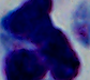

magnification = 1000x
modality = photomicrograph
identification = leukocyte